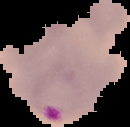
image type = cell region segmented out of the field of view; surrounding area masked to black
result = malaria parasites identified
preparation = thin blood smear
image size = 130×127 pixels